Name the parasite shown.
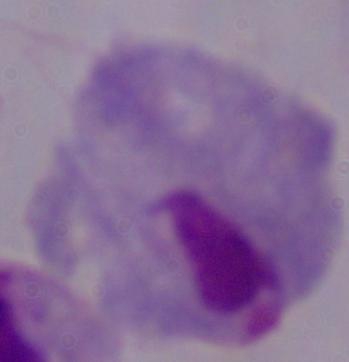
A trichomonad.

modality = photomicrograph
magnification = 1000x